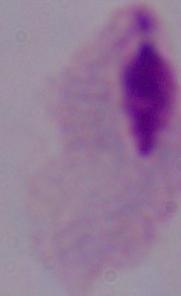
Summary:
  - Magnification: 1000x
  - Identification: trichomonad
  - Modality: photomicrograph